Assess the morphology of the erythrocytes.
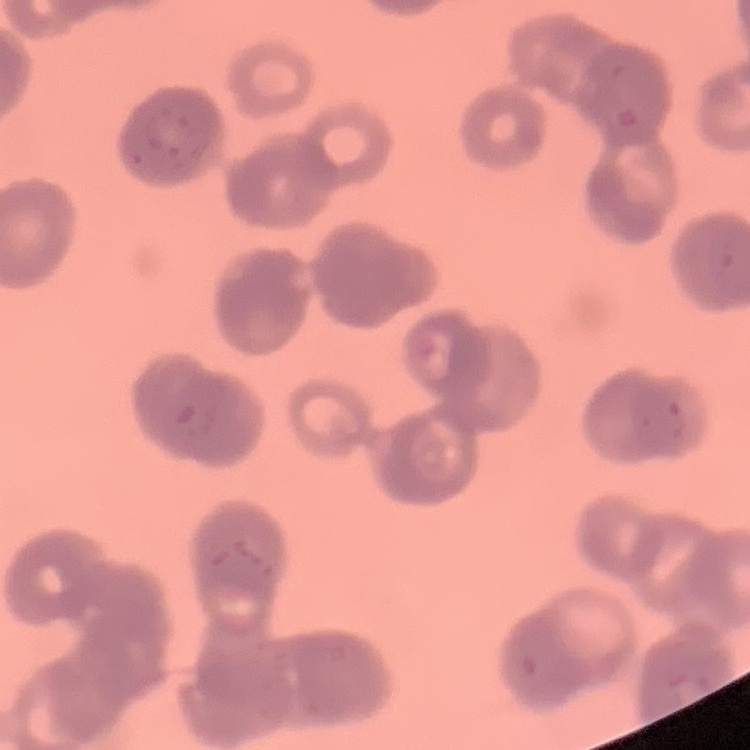

Rouleaux formation.

Thin peripheral smear. Square crop of a larger photomicrograph. Field's or Giemsa stain.